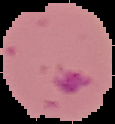 Result: Plasmodium parasites identified. The area outside the segmented cell region is set to black. Image is 115×124 pixels. From a thin blood smear.